Report the malaria status of this cell.
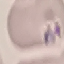

It is uninfected.

Acquired by smartphone through the microscope eyepiece. Thin blood film. Giemsa-stained preparation. Cell patch, automatically extracted from a larger field of view and resized to 64 × 64 pixels.